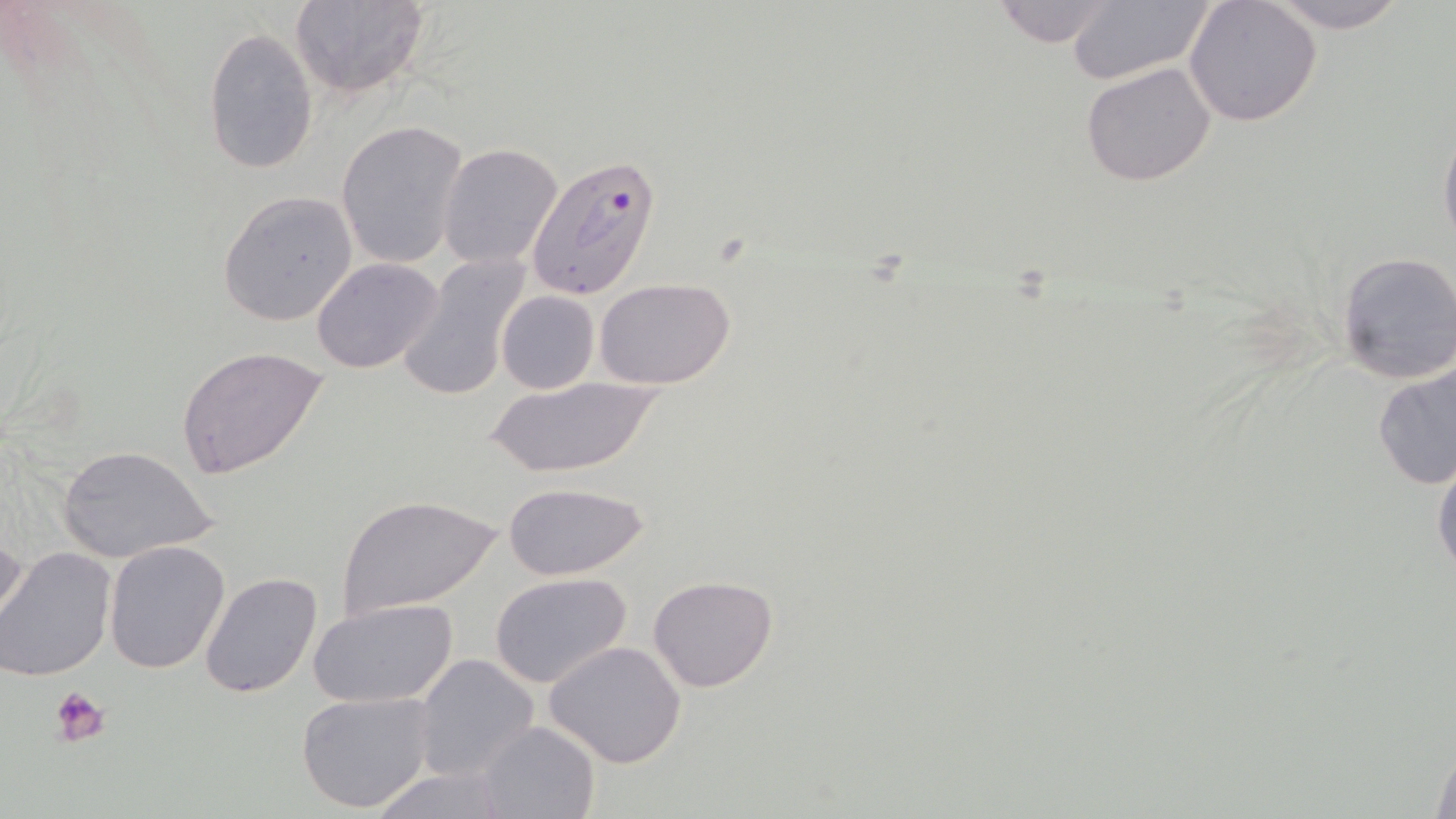 Approximate bounding boxes as named x1/y1/x2/y2 corners in pixels. Uninfected red blood cell locations: (x1=288, y1=0, x2=430, y2=99), (x1=987, y1=0, x2=1126, y2=48), (x1=1257, y1=0, x2=1416, y2=31), (x1=1063, y1=1, x2=1217, y2=87), (x1=1184, y1=1, x2=1322, y2=127), (x1=203, y1=27, x2=319, y2=176), (x1=1080, y1=61, x2=1219, y2=187), (x1=1439, y1=118, x2=1456, y2=259), (x1=337, y1=121, x2=468, y2=270), (x1=439, y1=142, x2=564, y2=269), (x1=218, y1=190, x2=359, y2=327), (x1=1335, y1=249, x2=1456, y2=385), (x1=397, y1=254, x2=533, y2=402), (x1=312, y1=258, x2=443, y2=373), (x1=594, y1=277, x2=738, y2=388), (x1=497, y1=290, x2=599, y2=394), (x1=176, y1=345, x2=331, y2=479), (x1=1372, y1=356, x2=1455, y2=492), (x1=484, y1=373, x2=665, y2=480), (x1=58, y1=445, x2=216, y2=566), (x1=1431, y1=448, x2=1456, y2=582), (x1=502, y1=481, x2=651, y2=582), (x1=336, y1=494, x2=502, y2=619), (x1=0, y1=526, x2=27, y2=637), (x1=103, y1=541, x2=230, y2=674), (x1=0, y1=549, x2=118, y2=681), (x1=198, y1=570, x2=324, y2=699), (x1=489, y1=572, x2=632, y2=689), (x1=648, y1=574, x2=778, y2=692), (x1=309, y1=600, x2=455, y2=708), (x1=544, y1=639, x2=689, y2=770), (x1=414, y1=653, x2=540, y2=783), (x1=296, y1=690, x2=435, y2=814), (x1=476, y1=721, x2=600, y2=818), (x1=1427, y1=731, x2=1456, y2=819), (x1=367, y1=764, x2=515, y2=819). Platelet locations: (x1=51, y1=685, x2=113, y2=747). Plasmodium falciparum-infected red blood cell locations: (x1=526, y1=151, x2=662, y2=300). Slide-level diagnosis: Plasmodium falciparum. One field of a larger specimen. Thin blood smear. Captured at 1000x magnification. May-Grünwald-Giemsa stain. Image is 1456×819 pixels. Optical microscopy.